Report the malaria status of this cell.
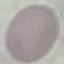

Uninfected.

image type = automatically extracted cell patch, resized to 64 × 64 pixels
preparation = thin blood film
capture = smartphone through the microscope eyepiece
stain = Giemsa